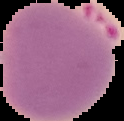

From a thin blood smear. Image is 124×121 pixels. Result: Plasmodium parasites identified. The area outside the segmented cell region is set to black.